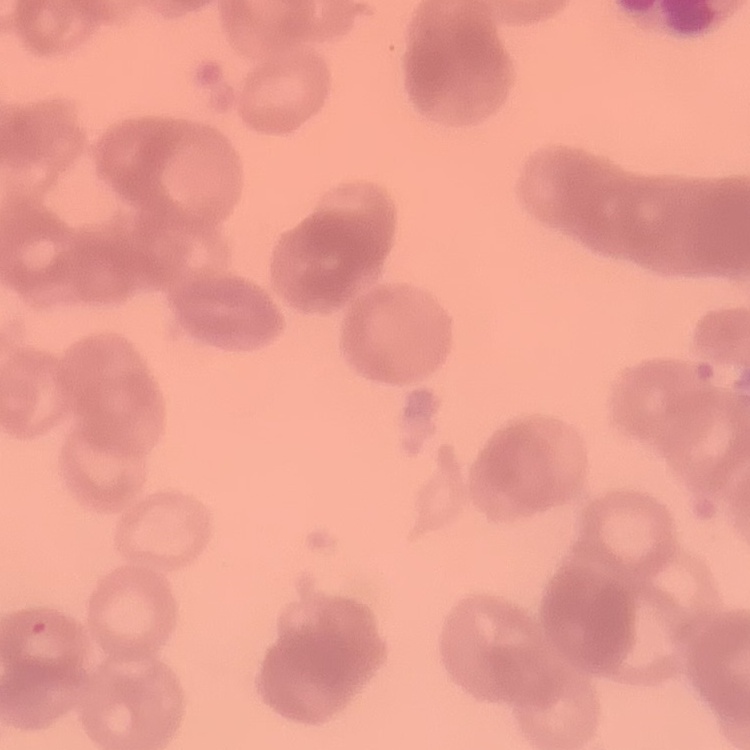
red blood cell morphology = rouleaux formation
image type = square crop of a larger photomicrograph
preparation = thin blood smear
stain = Field's or Giemsa